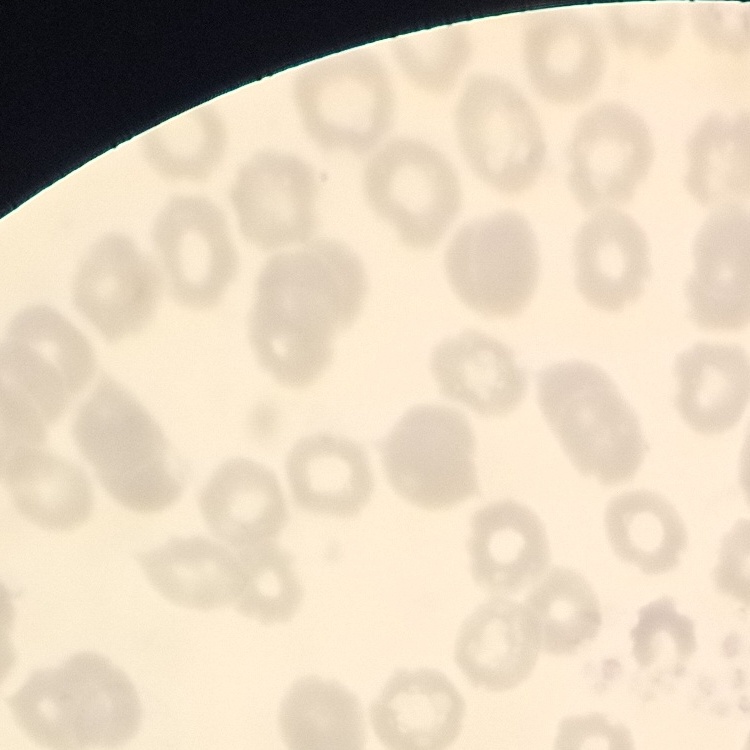 The erythrocytes exhibit no rouleaux formation. Thin blood film. One tile cut from a larger photomicrograph. Stained with either Field's or Giemsa.